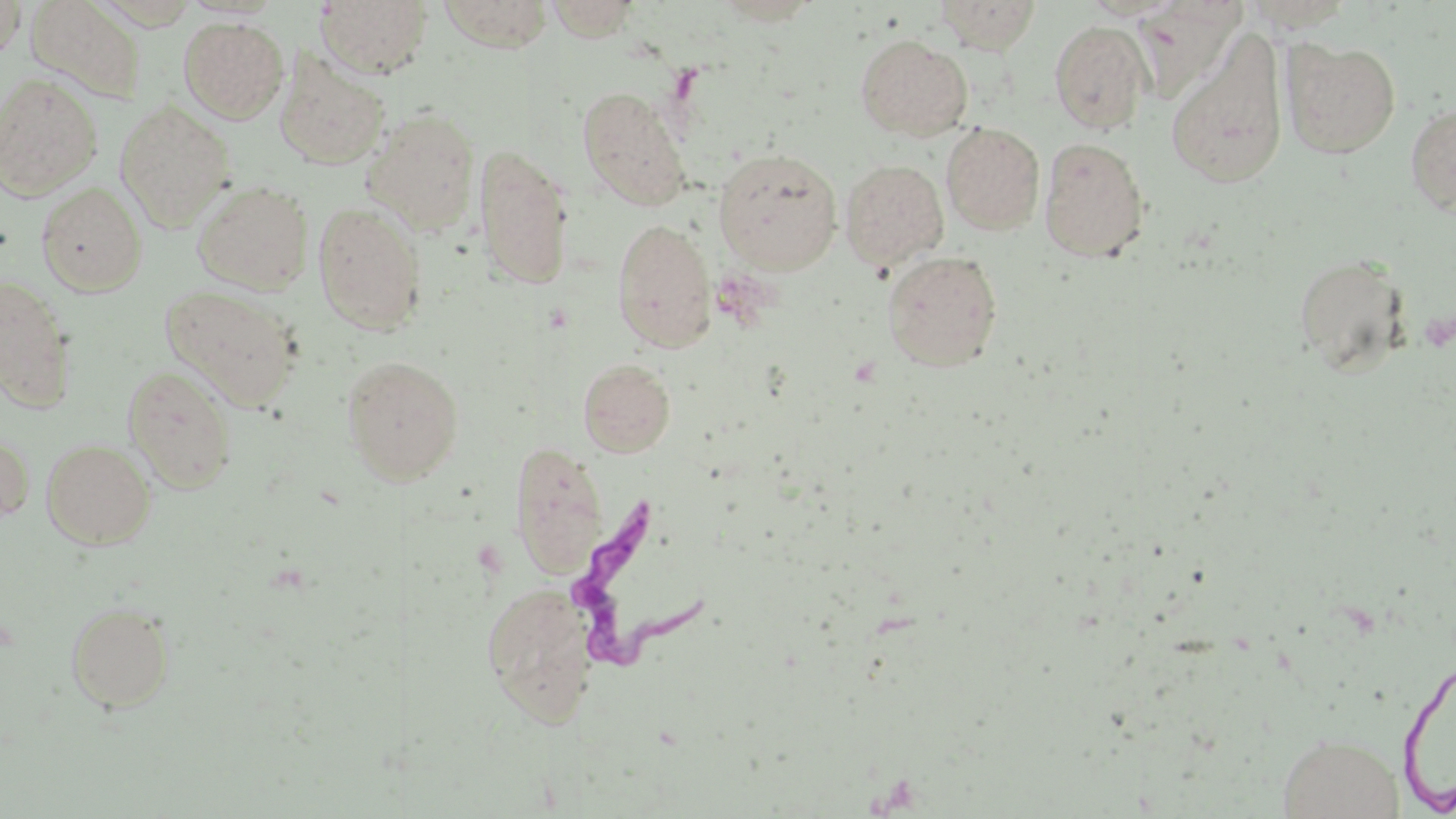
Approximate bounding boxes as [x1, y1, x2, y2] in pixels. Trypanosoma brucei locations: [564, 501, 719, 676]. Uninfected red blood cell locations: [314, 0, 435, 78], [541, 0, 643, 41], [933, 0, 1043, 53], [1, 1, 25, 64], [24, 1, 148, 106], [1239, 1, 1354, 32], [178, 16, 289, 124], [1049, 20, 1152, 134], [1165, 32, 1289, 190], [855, 34, 973, 141], [1282, 39, 1401, 158], [275, 55, 390, 169], [0, 73, 103, 200], [578, 87, 690, 210], [114, 98, 237, 232], [1405, 102, 1456, 216], [362, 108, 482, 235], [941, 122, 1045, 234], [1038, 138, 1149, 263], [473, 144, 576, 291], [712, 147, 843, 273], [840, 160, 949, 270], [192, 179, 315, 295], [36, 181, 148, 297], [312, 201, 428, 336], [612, 218, 716, 352], [882, 251, 1003, 371], [1293, 253, 1411, 376], [0, 274, 78, 412], [159, 284, 304, 411], [342, 355, 464, 485], [578, 358, 676, 458], [122, 364, 238, 493], [0, 431, 35, 526], [41, 438, 156, 549], [509, 439, 610, 580], [480, 582, 600, 726], [66, 600, 175, 712], [1276, 734, 1406, 817]. Slide-level diagnosis: Trypanosoma brucei. Image is 1456×819 pixels. 1000x magnification. Optical microscopy. May-Grünwald-Giemsa-stained preparation. Single field of view. Thin blood film.